Locate platelets.
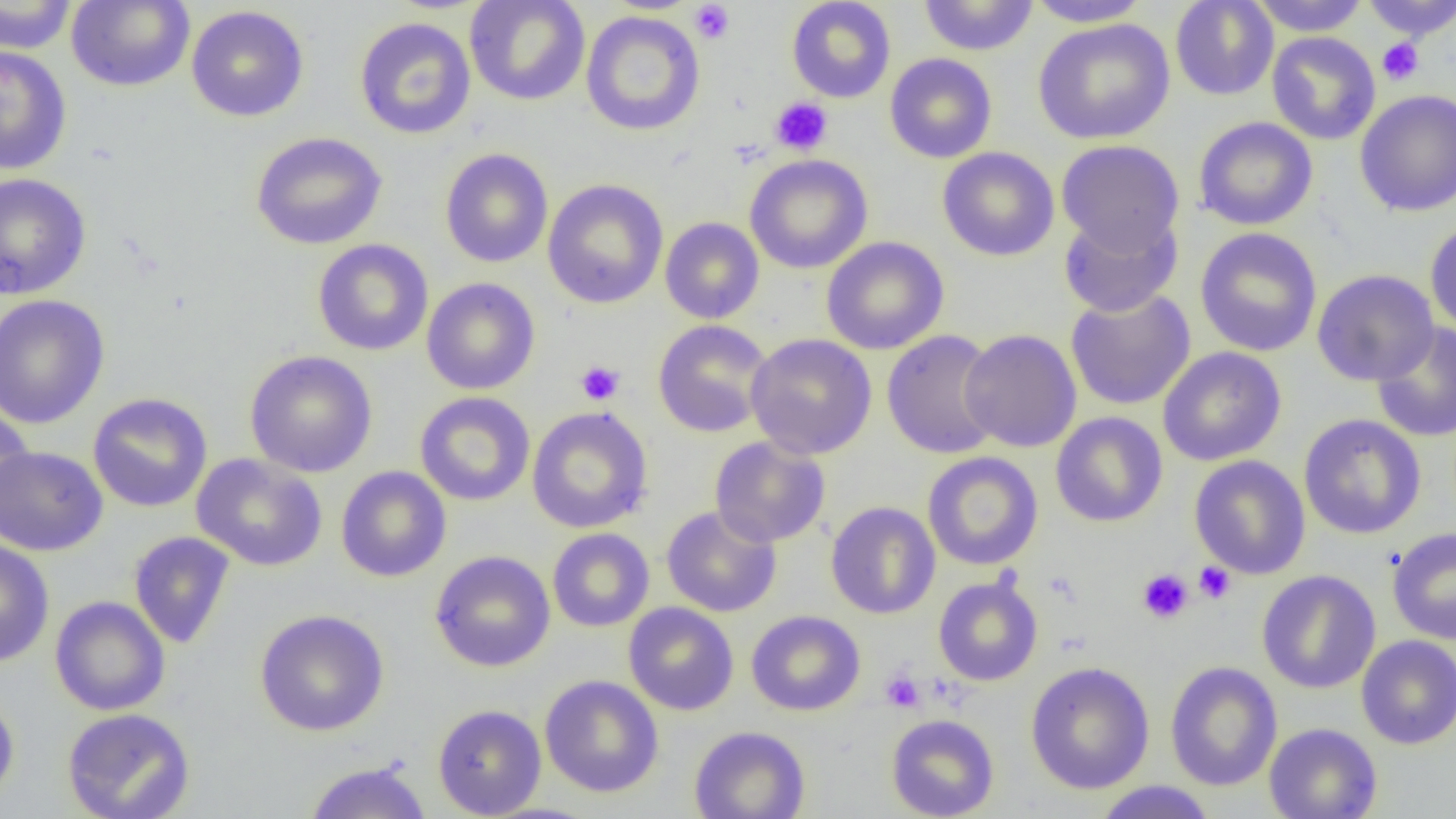

Approximate bounding boxes as [x1, y1, x2, y2] in pixels.
Platelets: [690, 1, 735, 44], [1377, 38, 1424, 86], [770, 97, 833, 156], [575, 360, 625, 405], [1193, 561, 1236, 604], [1136, 569, 1194, 624], [880, 669, 926, 714].

{
  "slide_level_diagnosis": "negative for blood parasites",
  "image_size": "1456×819 pixels",
  "preparation": "thin blood smear",
  "magnification": "1000x",
  "uninfected_red_blood_cell_locations": "approximate bounding boxes as [x1, y1, x2, y2] in pixels: [0, 0, 79, 54], [66, 0, 195, 92], [465, 0, 590, 106], [786, 0, 896, 103], [918, 0, 1038, 56], [1024, 0, 1154, 27], [1170, 0, 1278, 100], [1249, 0, 1370, 36], [1360, 0, 1456, 40], [186, 5, 309, 122], [581, 11, 705, 136], [355, 17, 477, 140], [1032, 18, 1175, 145], [1267, 31, 1381, 145], [0, 46, 72, 175], [884, 53, 997, 163], [1355, 89, 1456, 216], [1193, 117, 1319, 231], [250, 132, 388, 250], [1056, 140, 1184, 255], [937, 147, 1060, 262], [440, 148, 553, 268], [745, 154, 873, 274], [0, 173, 92, 300], [542, 179, 668, 309], [1058, 211, 1182, 318], [660, 217, 765, 324], [1425, 220, 1456, 335], [1195, 227, 1322, 357], [821, 236, 948, 354], [312, 239, 434, 356], [1312, 269, 1439, 387], [421, 277, 540, 395], [1065, 289, 1196, 411], [0, 294, 111, 429], [652, 320, 773, 438], [1371, 322, 1456, 443], [959, 329, 1082, 452], [881, 330, 1003, 460], [745, 333, 877, 459], [1158, 347, 1286, 466], [245, 350, 378, 477], [87, 392, 213, 513], [414, 392, 535, 507], [0, 404, 34, 523], [527, 407, 653, 533], [1051, 411, 1168, 528], [1298, 414, 1426, 539], [709, 436, 831, 547], [0, 445, 108, 556], [922, 451, 1043, 570], [191, 453, 328, 572], [1189, 455, 1310, 579], [336, 466, 451, 582], [825, 501, 940, 619], [661, 505, 782, 617], [547, 528, 654, 632], [1387, 528, 1456, 644], [128, 531, 236, 650], [0, 538, 55, 667], [430, 550, 556, 672], [1257, 570, 1380, 694], [933, 575, 1043, 686], [50, 596, 171, 716], [624, 602, 739, 716], [254, 609, 390, 736], [746, 610, 865, 716], [1356, 635, 1456, 749], [1025, 661, 1155, 795], [1165, 661, 1282, 791], [540, 675, 664, 798], [0, 688, 20, 809], [432, 704, 547, 818], [62, 708, 195, 819], [885, 714, 999, 819], [1264, 723, 1382, 819], [689, 726, 811, 819], [303, 759, 432, 818], [1092, 781, 1218, 818]",
  "field_of_view": "single",
  "modality": "light microscopy"
}